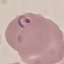
Malaria status: parasitized. Giemsa stain. Thin blood smear. Photographed with a smartphone camera at the microscope eyepiece. Cell patch, automatically extracted from a larger field of view and resized to 64 × 64 pixels.